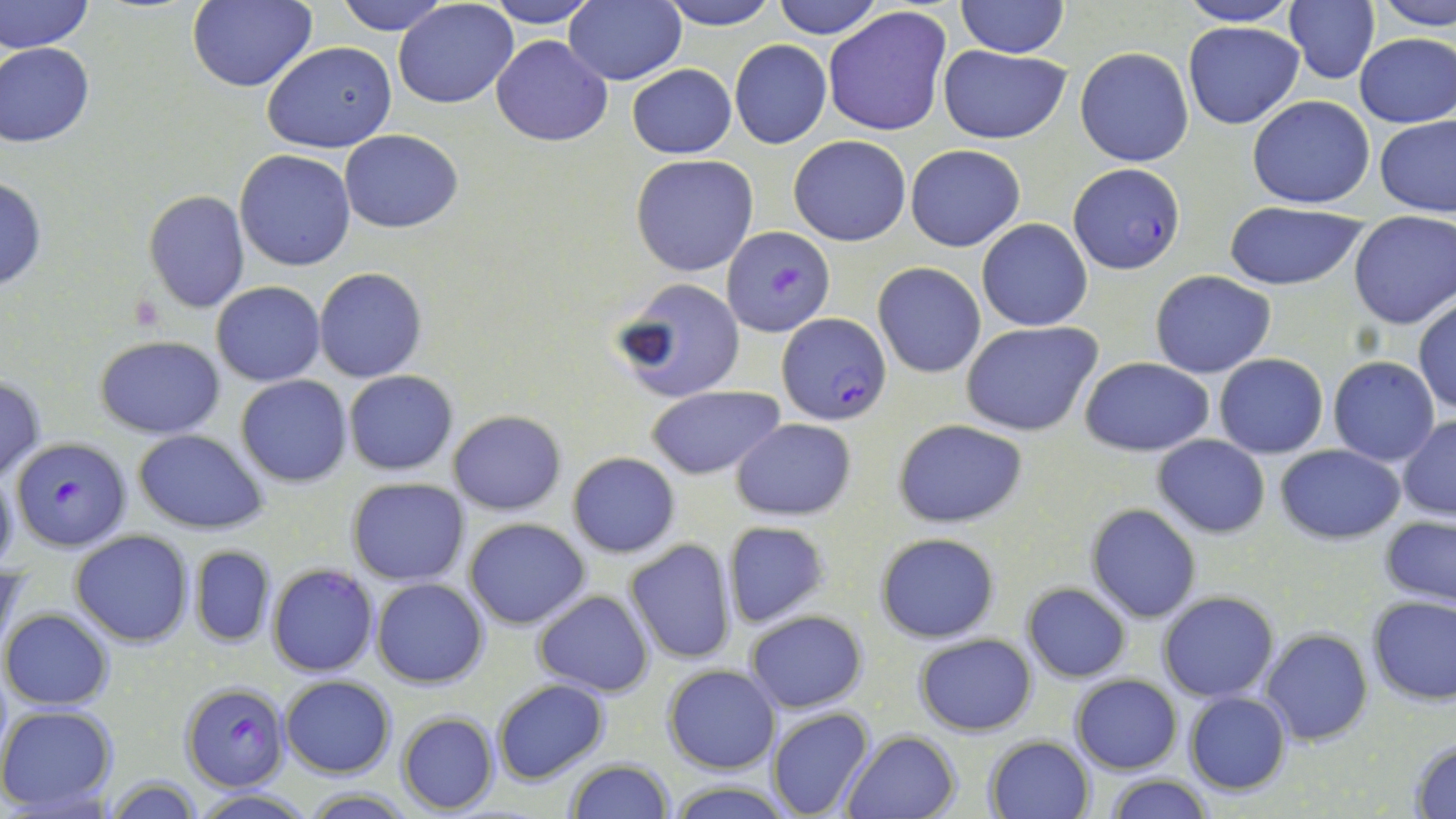
Summary:
  - Coordinate format: approximate bounding boxes as (x1,y1)-(x2,y2) corner pairs in pixels
  - Plasmodium falciparum-infected red blood cell locations: (1067,164)-(1185,275), (724,225)-(833,338), (777,313)-(890,424), (11,436)-(132,551), (181,681)-(289,791)
  - Uninfected red blood cell locations: (0,0)-(93,54), (187,0)-(317,93), (335,0)-(450,33), (481,0)-(600,27), (567,0)-(687,84), (657,0)-(783,28), (769,0)-(884,39), (956,0)-(1069,58), (1284,0)-(1380,85), (1376,0)-(1456,28), (394,1)-(519,108), (1177,1)-(1301,26), (822,6)-(951,138), (1183,20)-(1304,128), (1354,33)-(1456,127), (492,35)-(613,146), (729,39)-(831,149), (0,40)-(96,147), (261,40)-(397,154), (939,45)-(1070,144), (1076,46)-(1193,166), (627,64)-(737,159), (1247,94)-(1374,209), (1375,113)-(1456,216), (340,130)-(464,232), (788,135)-(911,246), (905,143)-(1026,251), (234,149)-(356,272), (630,154)-(760,277), (0,178)-(48,292), (142,190)-(249,313), (1225,202)-(1369,290), (1349,212)-(1456,329), (977,219)-(1091,331), (873,261)-(985,379), (314,267)-(426,383), (1149,270)-(1275,378), (614,276)-(746,404), (211,281)-(325,385), (1412,297)-(1456,415), (961,320)-(1103,436), (96,335)-(224,439), (1213,353)-(1328,458), (1081,355)-(1212,455), (1328,357)-(1440,465), (344,371)-(457,476), (0,375)-(46,484), (236,376)-(352,487), (646,386)-(785,478), (448,409)-(566,515), (1398,415)-(1456,520), (731,418)-(855,519), (894,420)-(1027,527), (133,429)-(267,533), (1154,433)-(1270,539), (1275,443)-(1404,544), (567,452)-(680,558), (0,467)-(18,575), (348,478)-(470,584), (1085,503)-(1201,622), (1380,516)-(1456,607), (464,517)-(591,630), (723,521)-(830,629), (71,531)-(193,647), (876,533)-(999,642), (625,538)-(737,665), (188,545)-(275,647), (266,564)-(379,678), (372,577)-(489,689), (1021,582)-(1132,682), (534,591)-(654,695), (1159,591)-(1279,703), (1367,595)-(1456,705), (2,608)-(114,709), (745,609)-(868,713), (1261,629)-(1371,745), (914,633)-(1038,736), (663,664)-(781,773), (279,675)-(396,778), (1070,675)-(1181,774), (492,678)-(610,784), (1183,692)-(1291,795), (0,704)-(119,813), (767,708)-(876,819), (396,712)-(498,814), (842,730)-(961,819), (984,734)-(1093,818), (1408,736)-(1456,817), (565,758)-(674,818), (1104,775)-(1214,819), (104,778)-(203,817), (662,781)-(798,818), (300,787)-(421,818), (192,788)-(316,819)
  - Slide-level diagnosis: Plasmodium falciparum
  - Preparation: thin blood smear
  - Stain: May-Grünwald-Giemsa
  - Modality: light microscopy
  - Field of view: one of a larger specimen
  - Magnification: 1000x
  - Image size: 1456×819 pixels